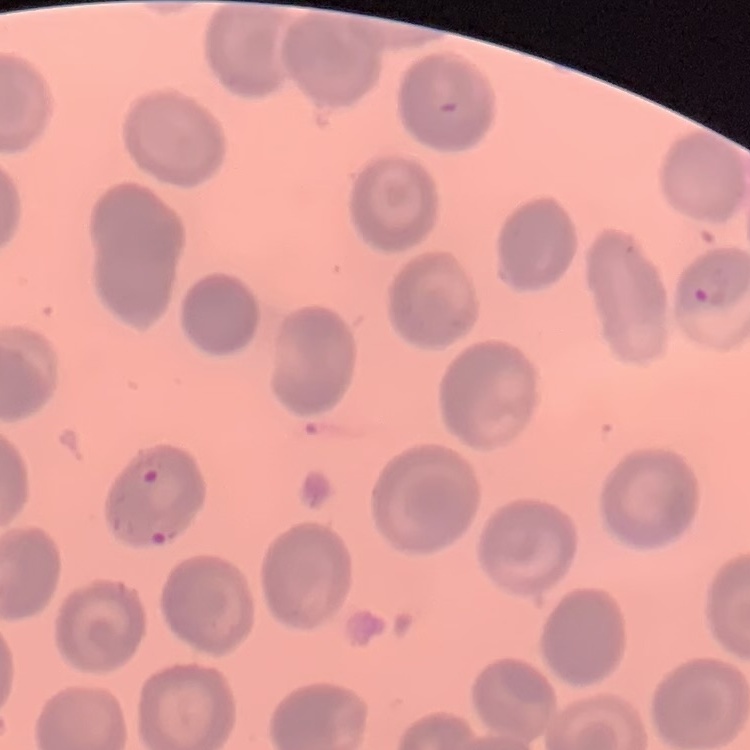

{
  "red_blood_cell_morphology": "no rouleaux formation",
  "preparation": "thin blood film",
  "image_type": "square crop of a larger photomicrograph",
  "stain": "Field's or Giemsa"
}